Report the malaria status of this cell.
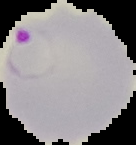
It is parasitized.

image size = 136×145 pixels
image type = segmented cell region with the area outside set to black
preparation = thin blood smear